Classify this cell by malaria status.
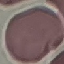
It is uninfected.

Thin blood film. Giemsa stain. Cell patch, automatically extracted from a larger field of view and resized to 64 × 64 pixels. Photographed with a smartphone camera at the microscope eyepiece.